Give the extent of all uninfected red blood cells.
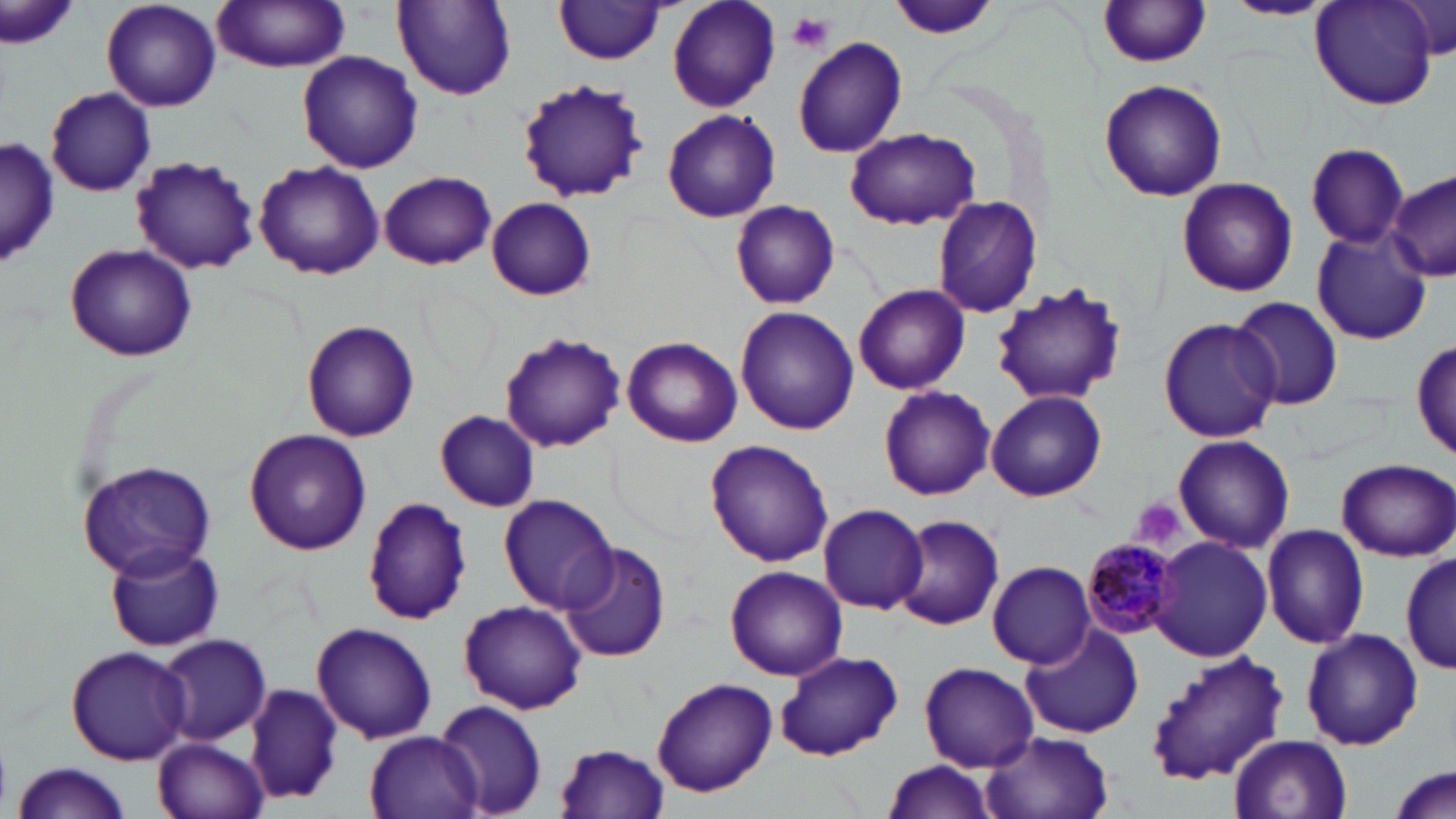
Approximate bounding boxes as (x1,y1)-(x2,y2) corner pairs in pixels.
Uninfected red blood cells: (100,0)-(221,112), (392,0)-(517,102), (555,0)-(668,63), (1224,0)-(1333,20), (212,1)-(352,72), (666,1)-(781,113), (1098,1)-(1213,69), (1312,1)-(1439,109), (2,2)-(77,56), (891,2)-(996,41), (1394,2)-(1453,58), (791,35)-(907,158), (297,51)-(423,174), (515,78)-(650,205), (1099,78)-(1228,203), (45,86)-(156,197), (662,108)-(781,224), (845,126)-(980,231), (1,137)-(58,272), (1307,143)-(1411,247), (129,155)-(259,274), (255,161)-(384,278), (378,170)-(496,270), (1389,172)-(1456,283), (1175,176)-(1299,297), (487,197)-(597,301), (933,197)-(1043,317), (731,200)-(840,309), (1311,230)-(1431,344), (65,243)-(197,360), (988,281)-(1131,406), (853,283)-(970,395), (1229,296)-(1343,410), (734,306)-(859,435), (1157,317)-(1282,444), (302,319)-(420,442), (498,332)-(626,453), (623,335)-(743,447), (1413,338)-(1455,456), (880,387)-(993,499), (986,390)-(1106,502), (434,410)-(541,511), (243,428)-(371,554), (1175,434)-(1294,552), (704,439)-(835,569), (77,457)-(218,580), (1338,459)-(1454,560), (499,495)-(619,614), (364,497)-(473,625), (817,503)-(928,614), (892,514)-(1005,632), (1261,523)-(1371,650), (1150,536)-(1273,661), (558,541)-(671,663), (106,542)-(225,652), (1401,550)-(1452,673), (989,561)-(1095,667), (726,567)-(848,679), (458,599)-(588,715), (1019,621)-(1146,738), (311,622)-(437,744), (1301,628)-(1423,751), (157,633)-(271,747), (65,645)-(192,764), (774,648)-(904,761), (1143,648)-(1290,788), (919,661)-(1039,771), (652,679)-(777,797), (244,681)-(345,806), (437,700)-(548,816), (982,729)-(1114,819), (365,731)-(483,817), (1229,734)-(1351,819), (155,736)-(269,819), (554,741)-(669,817), (879,759)-(997,817), (13,762)-(134,819), (1388,764)-(1454,818).

slide-level diagnosis = Plasmodium malariae
preparation = thin blood smear
modality = optical microscopy
Plasmodium malariae-infected red blood cell locations = approximate bounding boxes as (x1,y1)-(x2,y2) corner pairs in pixels: (1083,536)-(1183,636)
image size = 1456×819 pixels
platelet locations = approximate bounding boxes as (x1,y1)-(x2,y2) corner pairs in pixels: (789,12)-(836,54), (1128,498)-(1186,551)
magnification = 1000x
stain = May-Grünwald-Giemsa
field of view = one of a larger specimen